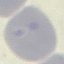
result = no malaria parasites detected
image type = automatically extracted cell patch, resized to 64 × 64 pixels
preparation = thin smear
stain = Giemsa
capture = smartphone camera at the microscope eyepiece